Assess the morphology of the erythrocytes.
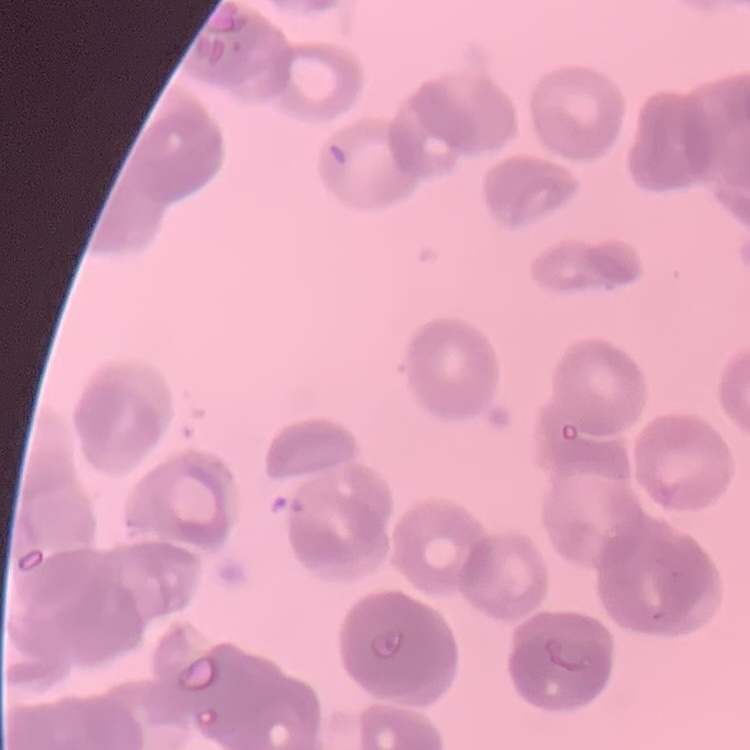
They show rouleaux formation.

One tile cut from a larger photomicrograph. Field's or Giemsa stain. Thin blood smear.